Report the malaria status of this cell.
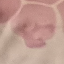

Uninfected.

preparation = thin blood smear
capture = smartphone camera at the microscope eyepiece
image type = cell patch, automatically extracted from a larger field of view and resized to 64 × 64 pixels
stain = Giemsa